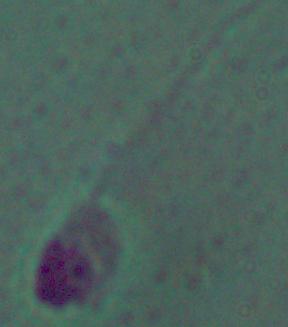

Captured at 1000x magnification. Photomicrograph. A Leishmania parasite is seen.